Evaluate for parasitized red blood cells.
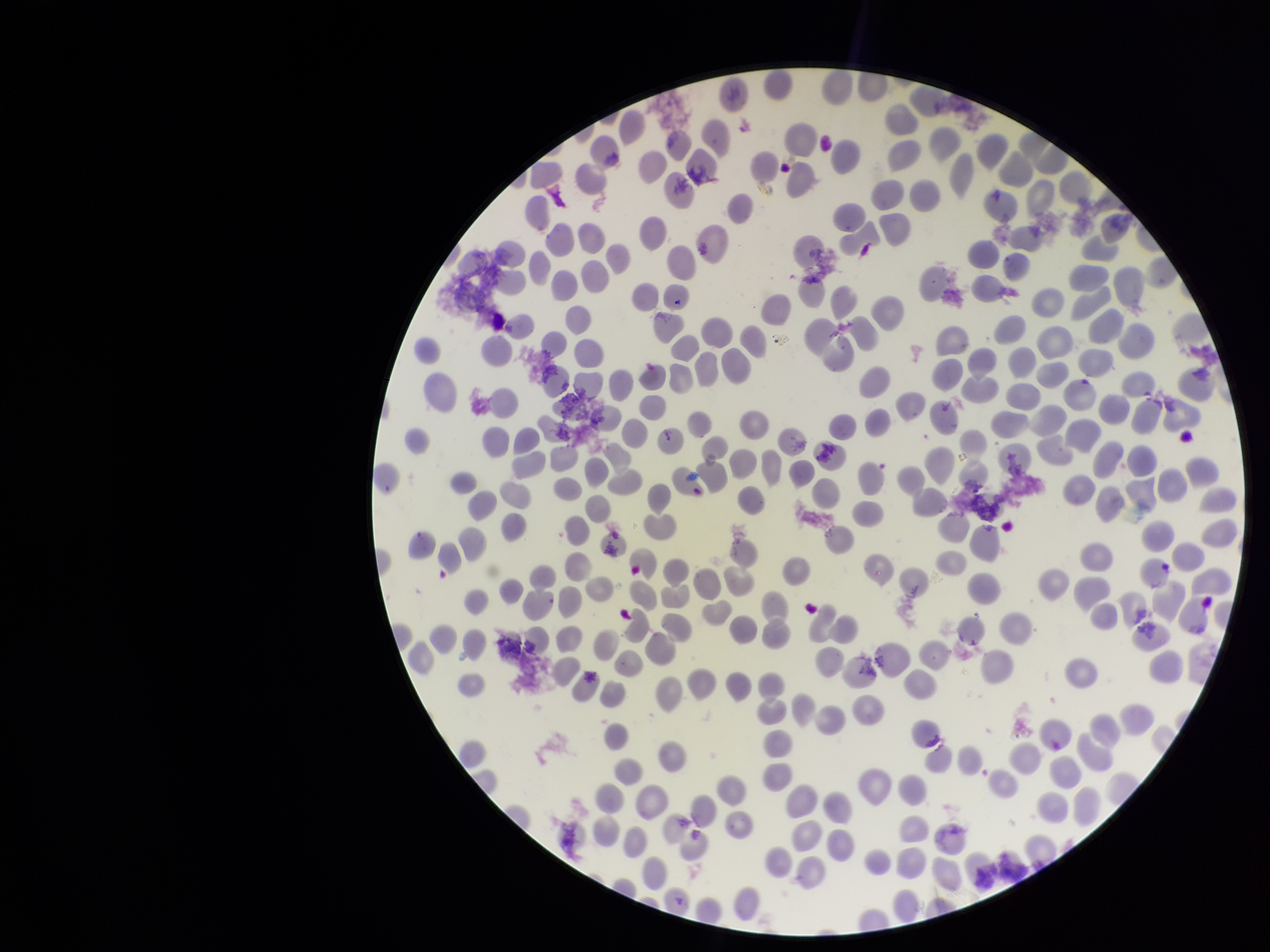

Seen.

Stained with Giemsa. Parasitized red blood cell count: 1. Preparation: thin smear. Species reported for this patient: Plasmodium vivax. Red blood cell count: 236. Image is 1270×952 pixels. Patient malaria status: infected. One field from this slide. Photographed through the microscope eyepiece with a smartphone camera.